Describe the morphology of the red blood cells.
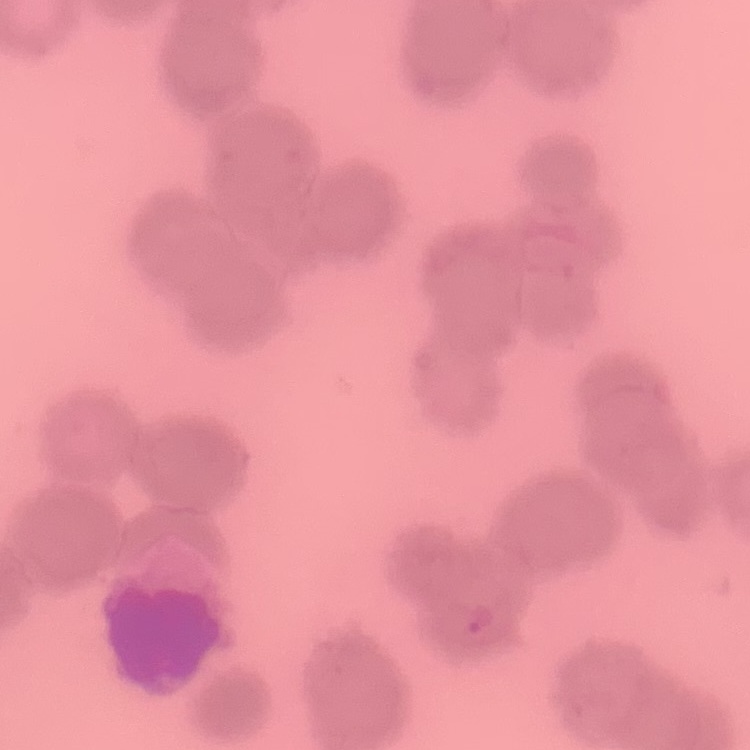
They show rouleaux formation.

Summary:
  - Preparation: thin blood smear
  - Stain: Field's or Giemsa
  - Image type: square crop of a larger photomicrograph